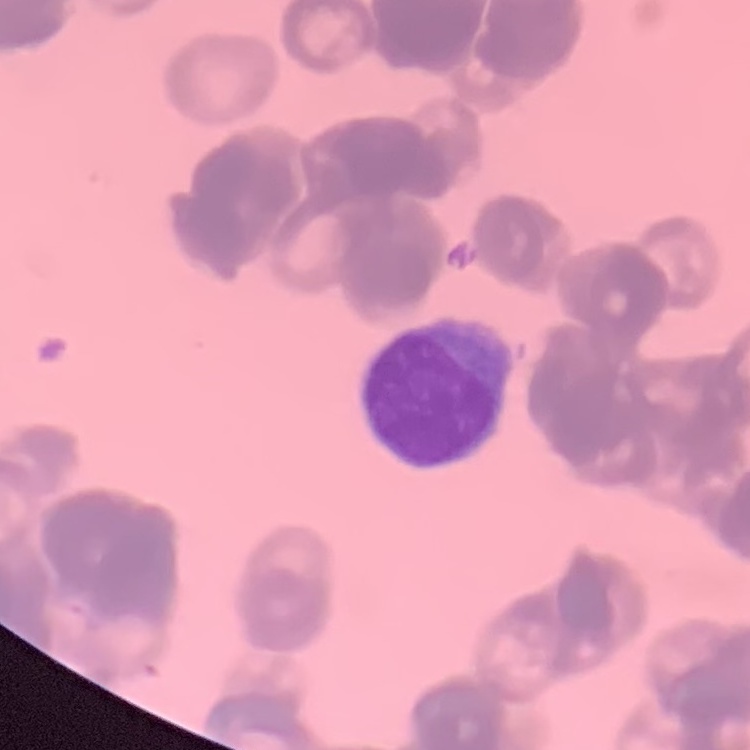
Summary:
  - Red blood cell morphology: rouleaux formation
  - Stain: Field's or Giemsa
  - Preparation: thin blood film
  - Image type: one tile cut from a larger photomicrograph